State which parasite is depicted.
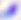
This is Toxoplasma gondii.

Micrograph. 400x magnification.